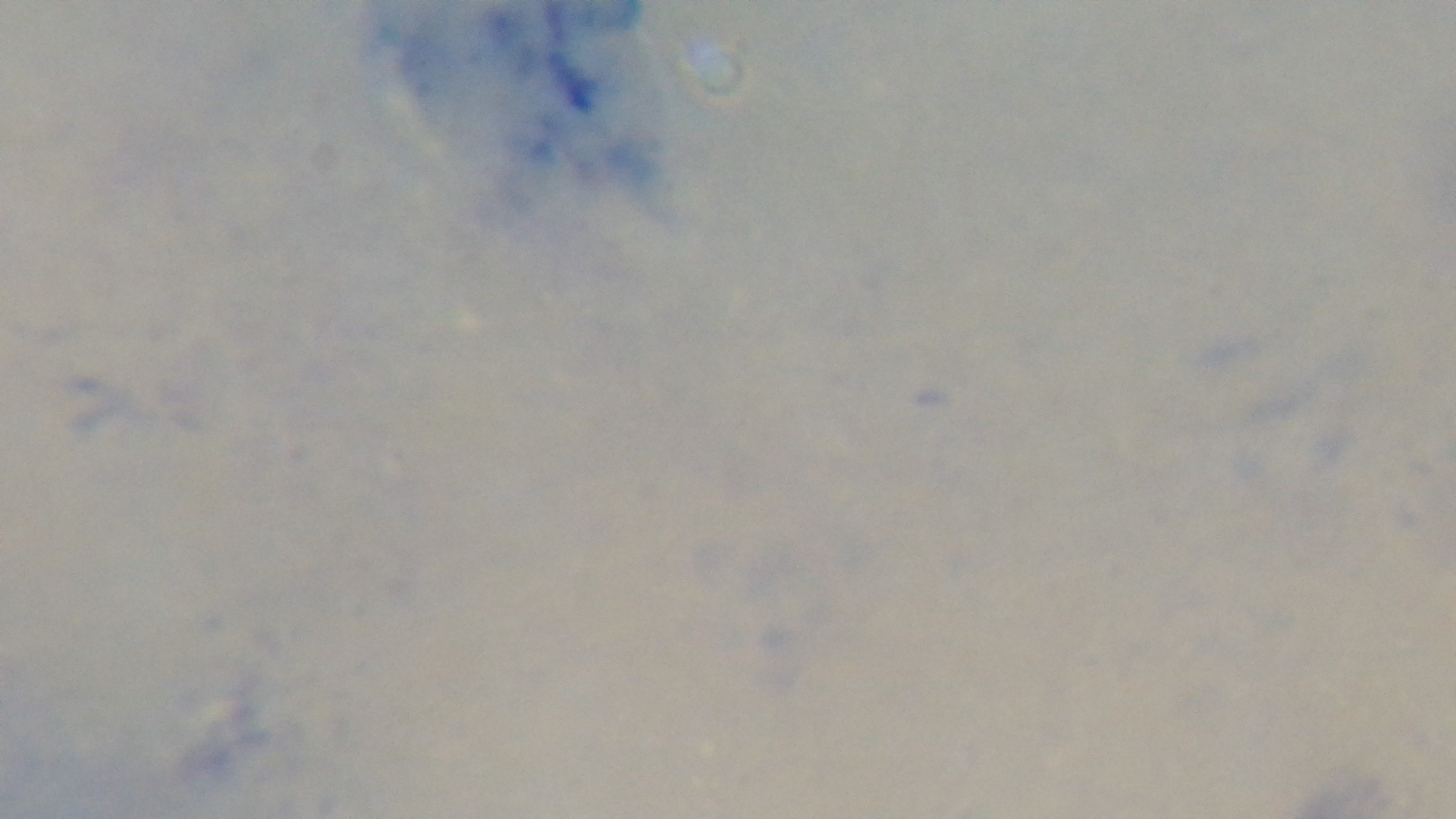
Preparation: thick. Giemsa stain. Light microscopy. Malaria status: negative. Mounted 4K digital camera. 100x oil-immersion objective. Single field of view.